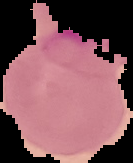 Image is 133×163 pixels. From a thin blood smear. The area outside the segmented cell region is set to black. Result: Plasmodium parasites detected.